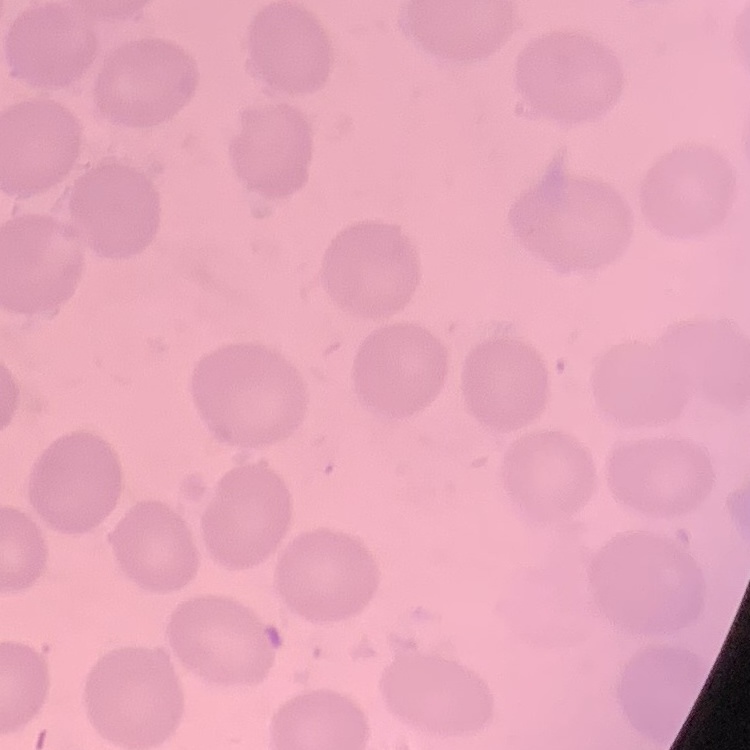

The erythrocytes exhibit no rouleaux formation. Thin peripheral smear. Field's or Giemsa stain. Square crop of a larger photomicrograph.